Report the malaria status.
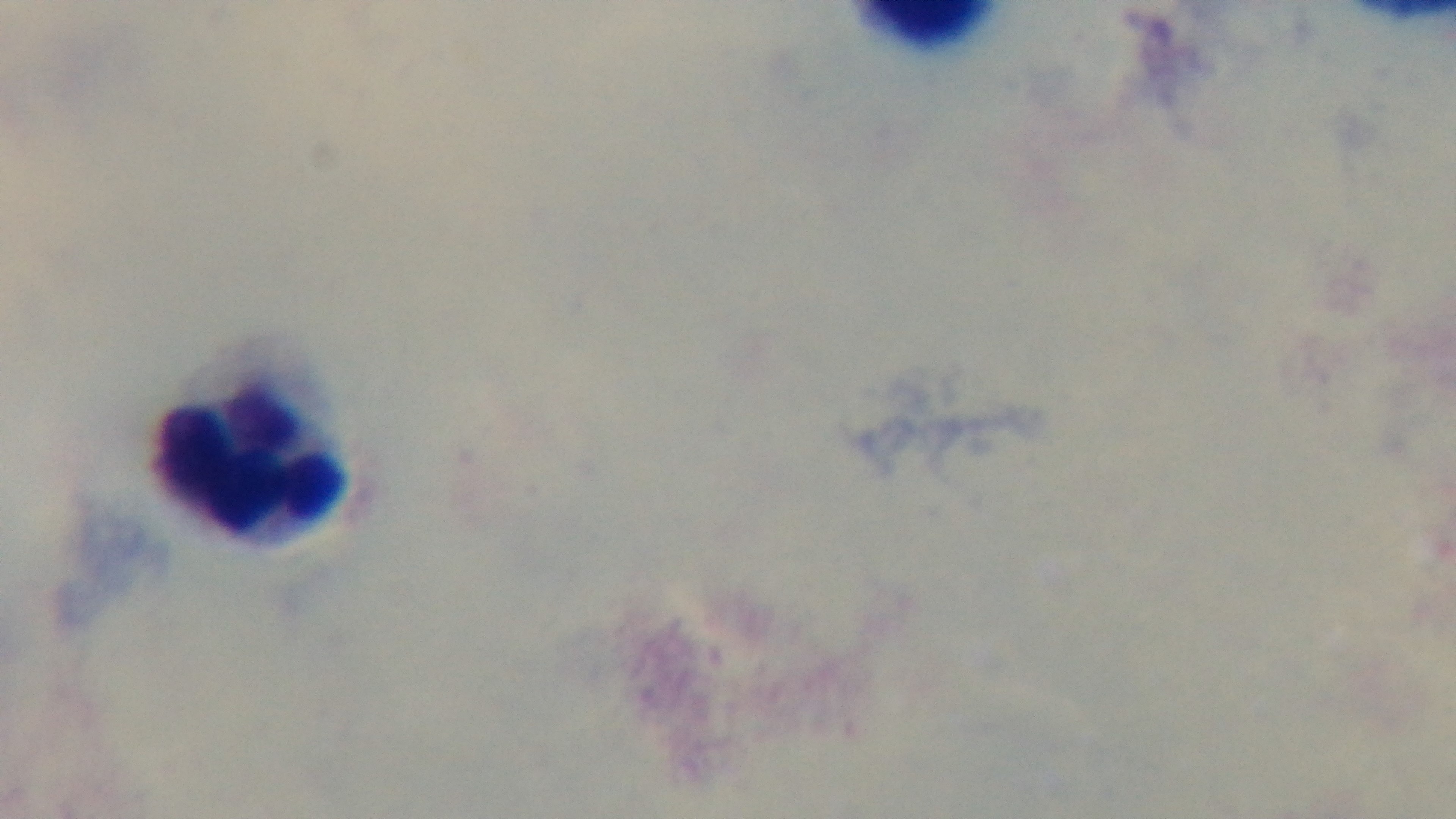
Negative.

Summary:
  - Capture: mounted 4K digital camera
  - Field of view: one from the slide
  - Preparation: thick
  - Stain: Giemsa
  - Modality: light microscopy
  - Objective: 100x oil immersion